Assess this cell for malaria.
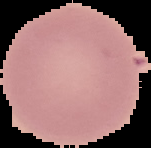

It is uninfected.

image size = 151×148 pixels
preparation = thin blood film
image type = segmented cell region with the area outside set to black